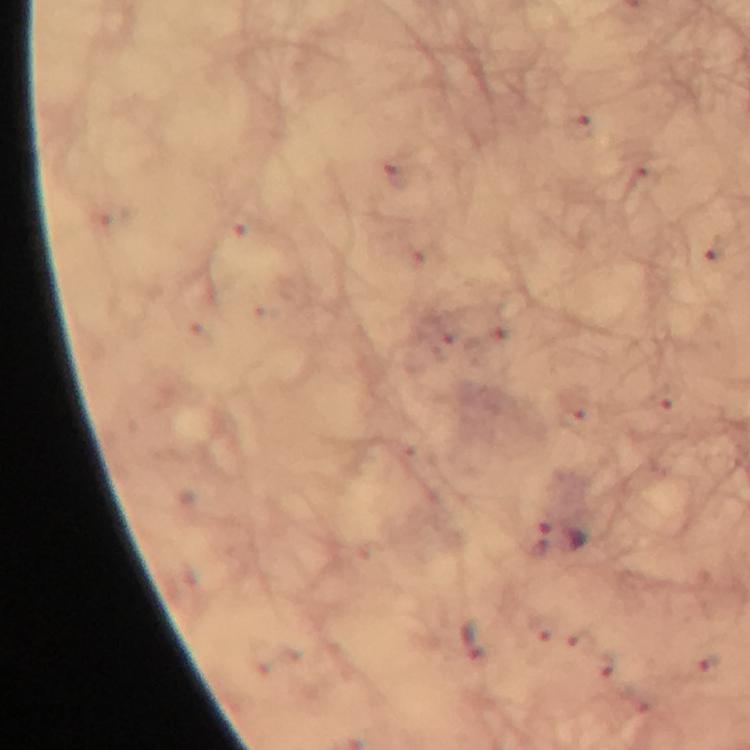
Approximate centers as {x, y} in pixels.
Summary:
  - Plasmodium parasite locations: {562, 539}, {473, 641}
  - Capture: smartphone camera through the microscope
  - Cropped from: one field of view
  - Context: from a diagnostic examination for malaria
  - Magnification: 100x
  - Stain: Giemsa
  - Preparation: thick blood film
  - Immersion oil: used
  - Image size: 750×750 pixels